Give a bounding box for every Plasmodium parasite.
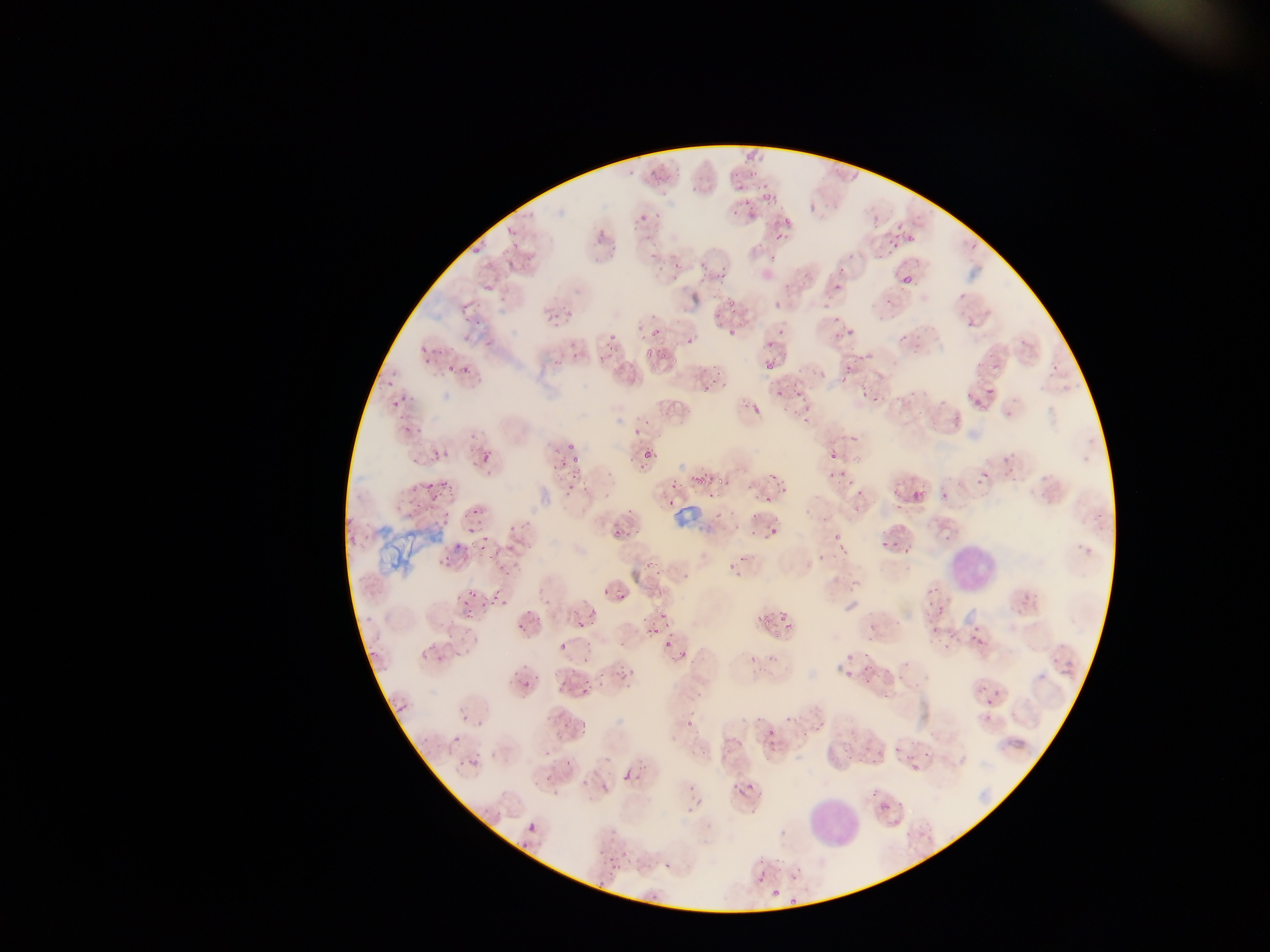
Approximate bounding boxes as left top right bottom in pixels.
Plasmodium parasites (some below the resolvable threshold): 745 155 753 162; 748 168 758 177; 649 169 658 177; 761 179 766 189; 650 180 668 186; 691 185 699 192; 762 190 773 199; 743 199 751 207; 732 210 741 218; 782 214 796 225; 639 215 647 222; 631 224 639 230; 505 225 513 236; 892 229 902 235; 775 231 782 240; 908 232 917 243; 643 235 652 241; 892 243 900 250; 883 246 894 258; 470 248 476 256; 769 254 776 262; 839 264 847 273; 892 269 903 279; 903 270 917 284; 714 271 725 285; 696 278 704 283; 783 281 793 288; 833 282 844 290; 884 296 891 304; 728 298 738 307; 714 312 722 320; 832 314 842 322; 966 321 975 329; 726 326 737 340; 847 326 858 336; 647 327 660 334; 899 332 910 345; 609 333 615 343; 687 337 696 345; 419 339 432 352; 764 339 773 350; 606 343 613 355; 660 349 667 359; 570 351 579 359; 646 352 654 360; 852 352 858 361; 598 354 606 361; 551 356 562 367; 671 356 680 365; 765 359 775 371; 462 362 475 376; 976 363 984 368; 991 364 999 372; 445 365 453 374; 844 365 852 379; 713 368 724 376; 385 379 394 387; 702 384 715 393; 984 387 997 395; 775 390 783 396; 874 397 884 402; 393 402 398 410; 972 403 977 411; 751 405 761 413; 404 421 413 432; 849 435 862 443; 566 445 575 451; 642 450 653 462; 483 453 493 463; 571 454 579 465; 628 457 636 463; 560 460 568 466; 767 468 778 479; 840 468 846 477; 830 470 836 478; 981 471 988 479; 569 472 581 478; 690 476 706 485; 715 476 728 484; 847 476 855 484; 425 480 434 489; 567 482 575 490; 670 482 678 488; 411 483 424 491; 782 486 790 493; 909 487 928 509; 856 489 866 495; 890 492 899 498; 763 494 776 505; 430 495 438 502; 706 495 714 501; 666 499 675 508; 473 505 481 514; 626 506 632 514; 1094 512 1105 519; 769 525 775 535; 614 526 623 538; 484 532 492 538; 832 536 840 540; 891 540 898 549; 835 543 843 549; 455 544 463 550; 901 546 912 555; 442 553 451 561; 739 553 747 562; 485 554 493 560; 651 557 655 566; 645 560 650 569; 497 564 504 572; 504 568 512 576; 601 585 610 596; 467 590 475 596; 493 592 500 602; 619 594 629 601; 458 599 468 604; 480 599 491 612; 653 604 663 612; 466 605 477 615; 588 608 596 615; 778 612 790 626; 659 613 669 618; 641 617 646 625; 760 618 768 628; 576 619 584 632; 517 620 523 628; 652 624 663 637; 931 627 939 634; 644 628 652 634; 773 629 782 639; 968 629 992 656; 948 631 956 639; 666 637 677 648; 617 639 625 648; 583 640 591 645; 428 643 442 650; 560 643 569 650; 679 646 688 656; 862 649 872 660; 418 650 430 658; 369 651 377 657; 437 652 445 660; 846 655 857 661; 580 657 588 664; 862 665 870 672; 623 666 636 676; 569 667 579 673; 845 670 856 681; 596 671 606 679; 617 673 626 681; 523 676 531 686; 557 680 569 692; 581 687 587 695; 881 694 889 700; 985 697 997 706; 397 702 408 711; 462 714 468 722; 476 717 482 727; 580 718 588 728; 811 721 818 732; 768 729 775 737; 800 733 811 738; 733 736 746 747; 842 744 847 752; 892 745 898 753; 543 747 554 757; 924 749 930 761; 860 753 868 764; 904 753 913 761; 847 754 852 762; 467 755 481 764; 565 758 573 766; 636 759 645 767; 873 759 879 768; 912 760 920 770; 622 767 630 779; 633 772 643 782; 544 774 555 786; 687 782 695 791; 748 782 755 790; 731 783 737 792; 871 789 877 797; 881 798 887 809; 685 806 694 817; 526 821 539 834; 606 856 621 872; 758 857 766 865; 665 859 674 869; 758 877 764 887; 596 883 605 891; 770 888 781 897; 788 895 796 904 | approximate x y pixel centers of objects too small to bound: 735 175; 739 188; 658 215; 652 257; 702 265; 675 266; 661 268; 805 273; 558 314; 556 323; 572 344; 862 356; 843 380; 864 395; 797 396; 966 396; 803 401; 981 406; 804 408; 956 419; 646 421; 805 421; 932 425; 636 433; 835 456; 641 468; 609 476; 978 483; 443 484; 757 495; 942 495; 896 507; 753 517; 737 527; 512 528; 468 530; 752 533; 631 535; 884 544; 482 549; 658 571; 503 601; 929 603; 528 610; 669 610; 524 630; 946 646; 456 654; 753 659; 887 671; 901 676; 587 680; 868 682; 600 683; 788 718; 759 720; 567 724; 688 724; 455 738; 585 783; 522 847; 613 874.

leukocyte locations = approximate bounding boxes as left top right bottom in pixels: 946 537 998 596; 801 794 864 855
field of view = single
image size = 1270×952 pixels
country = Ghana
capture = mobile-phone photograph through a microscope
preparation = thin blood film